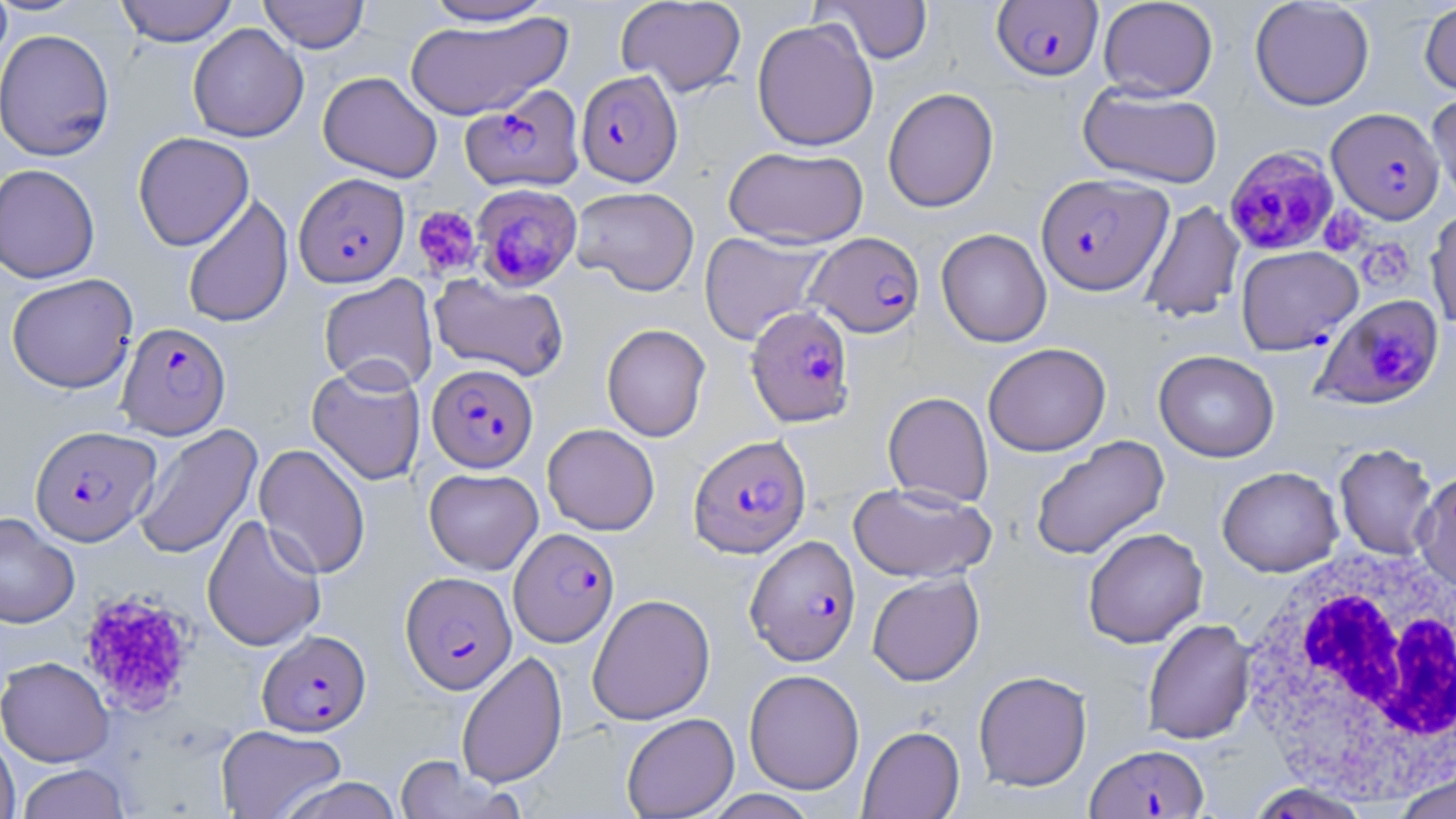
slide-level diagnosis = Plasmodium falciparum
white blood cell locations = approximate bounding boxes as (x1,y1)-(x2,y2) corner pairs in pixels: (1231,545)-(1456,801)
Plasmodium falciparum-infected red blood cell locations (subset) = approximate bounding boxes as (x1,y1)-(x2,y2) corner pairs in pixels: (991,1)-(1103,81), (576,70)-(683,186), (460,84)-(586,193), (1327,108)-(1445,223), (1225,144)-(1340,254), (294,173)-(409,287), (1036,173)-(1172,296), (471,184)-(584,291), (806,232)-(925,338), (1313,293)-(1444,409), (745,305)-(856,427), (117,322)-(230,439), (428,363)-(538,473), (30,425)-(160,546), (688,433)-(811,558), (745,535)-(861,666), (400,571)-(516,694), (257,629)-(371,736), (1086,743)-(1208,818)
preparation = thin blood film
modality = light microscopy
stain = May-Grünwald-Giemsa
magnification = 1000x
image size = 1456×819 pixels
uninfected red blood cell locations (subset) = approximate bounding boxes as (x1,y1)-(x2,y2) corner pairs in pixels: (0,0)-(12,72), (114,0)-(239,46), (258,0)-(370,53), (419,0)-(560,26), (616,0)-(747,96), (818,0)-(934,64), (1098,0)-(1218,101), (1249,0)-(1375,111), (1419,1)-(1456,96), (404,11)-(571,121), (752,18)-(878,151), (188,23)-(308,142), (0,29)-(115,161), (318,71)-(442,183), (1077,85)-(1223,188), (883,87)-(999,213), (1427,90)-(1456,213), (132,132)-(254,251), (723,145)-(869,249), (0,164)-(100,284), (570,186)-(700,295), (182,194)-(293,329), (1139,201)-(1245,322), (1426,206)-(1456,331), (936,228)-(1051,347), (698,231)-(831,346), (5,273)-(138,393), (429,273)-(570,381), (318,274)-(438,393), (602,323)-(711,442), (983,342)-(1111,456), (1153,350)-(1279,462), (307,362)-(426,486), (882,391)-(993,508), (133,423)-(263,560), (542,423)-(660,535), (1029,435)-(1170,561), (254,443)-(371,579), (1334,443)-(1438,560), (1217,466)-(1343,577), (848,481)-(996,582), (0,512)-(81,628), (202,515)-(326,652), (1082,527)-(1207,648), (867,572)-(984,686), (587,593)-(715,725), (1143,618)-(1256,744), (456,651)-(568,788), (0,656)-(114,767), (744,669)-(865,795), (973,670)-(1092,791), (621,712)-(739,818), (216,725)-(347,819), (858,725)-(965,819), (0,732)-(20,819), (393,755)-(521,819), (15,764)-(131,819), (1392,768)-(1456,819), (276,776)-(406,819), (1242,782)-(1377,819), (703,790)-(821,819)
platelet locations = approximate bounding boxes as (x1,y1)-(x2,y2) corner pairs in pixels: (412,205)-(482,278), (1318,206)-(1369,257), (1357,237)-(1416,292), (77,587)-(198,716)
field of view = single